Classify this cell by malaria status.
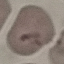

It is uninfected.

image type = automatically extracted cell patch, resized to 64 × 64 pixels
capture = smartphone through the microscope eyepiece
stain = Giemsa
preparation = thin smear